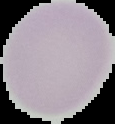

The area outside the segmented cell region is set to black. From a thin blood film. Malaria status: uninfected. Image is 115×124 pixels.